Classify this cell by malaria status.
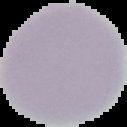
It is uninfected.

Summary:
  - Image size: 127×127 pixels
  - Preparation: thin blood smear
  - Image type: segmented cell region on a black background